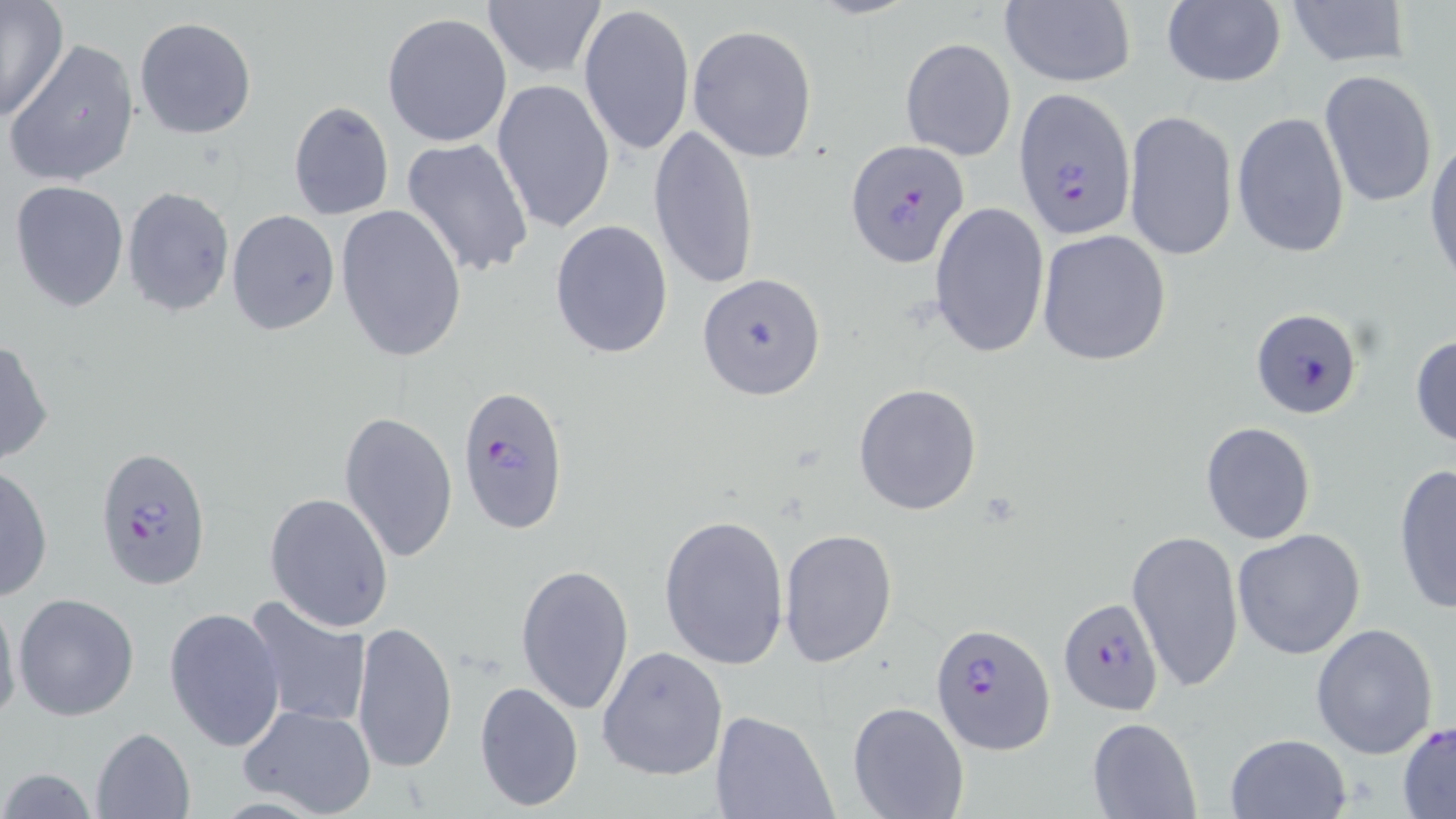 Approximate bounding boxes as [x1, y1, x2, y2] in pixels. Uninfected red blood cell locations: [1282, 0, 1410, 69], [482, 1, 607, 81], [1159, 1, 1287, 88], [0, 2, 70, 121], [998, 2, 1136, 88], [578, 4, 695, 158], [382, 12, 513, 146], [133, 17, 256, 139], [688, 25, 819, 162], [4, 38, 140, 188], [900, 38, 1016, 162], [1318, 69, 1439, 209], [491, 79, 617, 235], [288, 100, 394, 220], [1121, 108, 1237, 264], [1231, 110, 1351, 259], [649, 124, 760, 290], [1425, 135, 1456, 287], [401, 137, 535, 278], [10, 180, 128, 312], [121, 186, 234, 317], [929, 200, 1051, 360], [335, 203, 468, 365], [227, 208, 340, 334], [548, 219, 674, 358], [1035, 229, 1172, 366], [1410, 334, 1456, 450], [0, 337, 54, 466], [853, 383, 983, 516], [338, 410, 458, 565], [1200, 421, 1317, 544], [0, 464, 52, 601], [1392, 465, 1455, 616], [264, 492, 394, 633], [658, 513, 790, 670], [777, 526, 898, 669], [1232, 528, 1366, 661], [1126, 529, 1244, 694], [515, 562, 635, 715], [0, 590, 20, 730], [13, 593, 140, 721], [242, 596, 371, 730], [164, 605, 286, 752], [352, 619, 457, 775], [1310, 622, 1440, 760], [597, 646, 728, 781], [474, 680, 585, 812], [847, 700, 970, 819], [238, 705, 378, 818], [710, 708, 837, 819], [1086, 717, 1200, 818], [1398, 723, 1456, 816], [90, 727, 196, 818], [1225, 733, 1351, 818], [2, 766, 100, 819]. Plasmodium falciparum-infected red blood cell locations: [1019, 88, 1139, 240], [845, 140, 972, 268], [698, 273, 827, 400], [1251, 308, 1363, 420], [460, 382, 569, 535], [92, 442, 214, 590], [1057, 595, 1164, 714], [931, 622, 1055, 755]. Slide-level diagnosis: Plasmodium falciparum. May-Grünwald-Giemsa stain. Thin blood film. 1000x magnification. Light microscopy. Image is 1456×819 pixels. One field of a larger specimen.